Comment on the morphology of the erythrocytes.
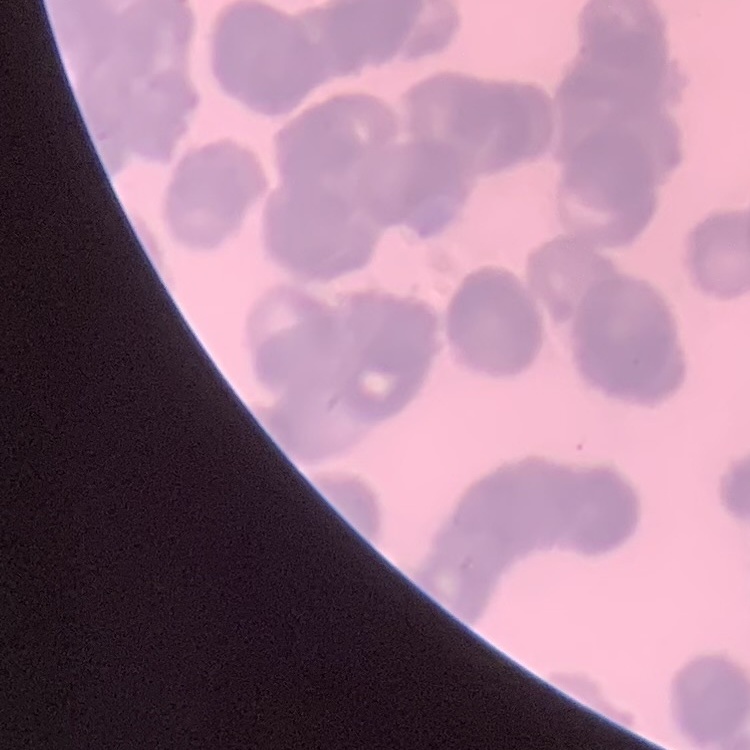
They show rouleaux formation.

stain = Field's or Giemsa
preparation = thin blood film
image type = one tile cut from a larger photomicrograph